Report the malaria status of this cell.
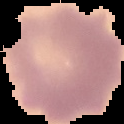

It is uninfected.

Summary:
  - Image size: 124×124 pixels
  - Image type: segmented cell region with the area outside set to black
  - Preparation: thin blood film